Identify the blood parasite species.
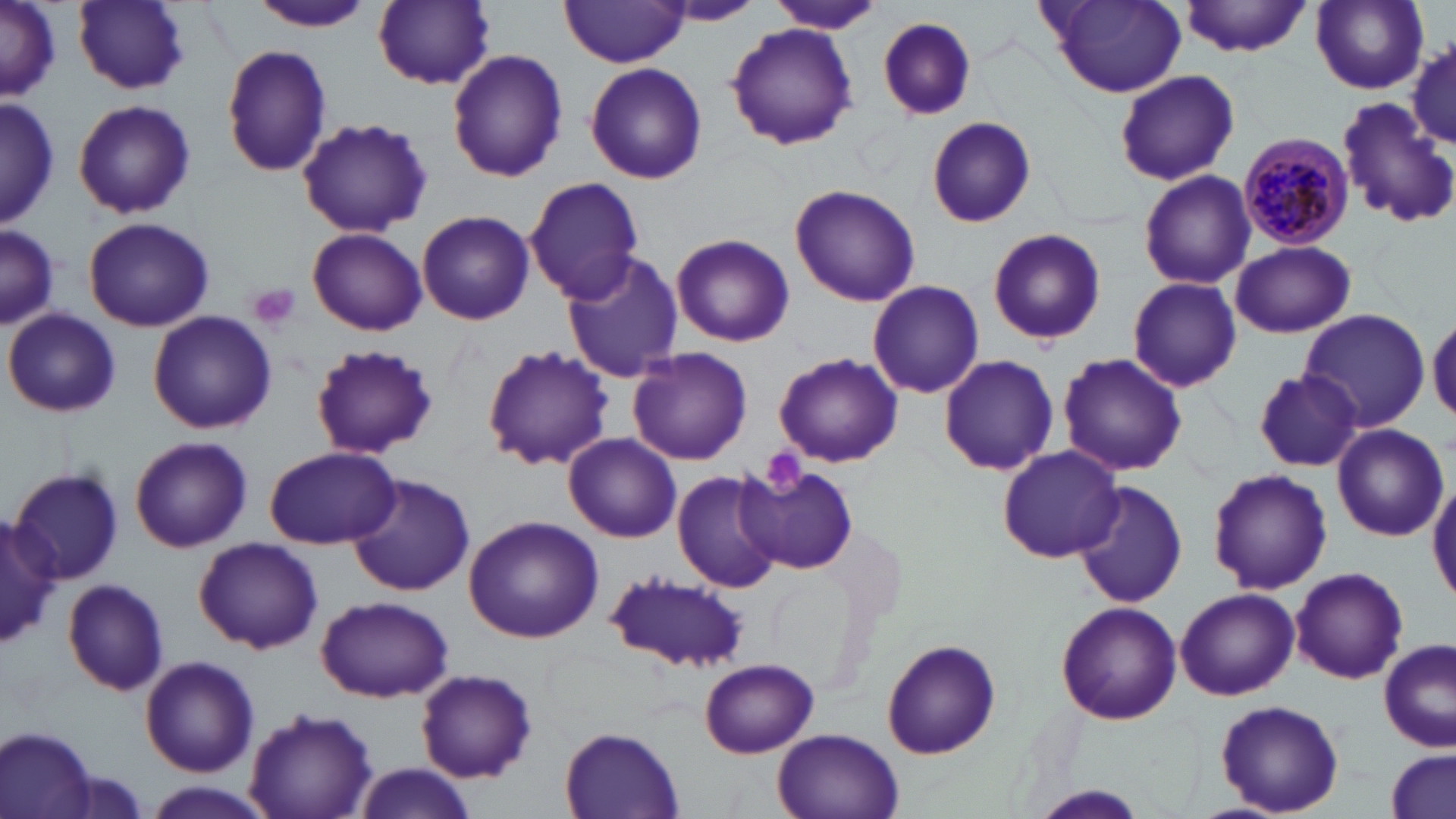
Plasmodium malariae.

Approximate bounding boxes as (x1,y1)-(x2,y2) corner pairs in pixels. Uninfected red blood cell locations: (0,0)-(59,103), (246,0)-(375,31), (373,0)-(496,88), (1042,0)-(1188,97), (1311,0)-(1429,92), (73,1)-(191,93), (1184,1)-(1312,56), (561,2)-(690,67), (666,2)-(763,24), (768,2)-(886,35), (879,16)-(978,120), (726,23)-(857,151), (1407,38)-(1456,151), (221,43)-(333,178), (446,49)-(569,182), (586,61)-(707,186), (1113,70)-(1240,184), (0,97)-(58,230), (1334,97)-(1455,230), (73,98)-(196,220), (928,116)-(1036,228), (296,118)-(433,238), (1138,169)-(1256,290), (525,176)-(647,303), (789,185)-(919,307), (417,209)-(535,325), (83,217)-(216,332), (0,226)-(59,329), (987,227)-(1106,346), (307,228)-(427,337), (671,233)-(794,347), (1229,240)-(1355,339), (560,250)-(684,382), (1127,276)-(1243,392), (869,281)-(984,399), (5,308)-(120,418), (1298,309)-(1430,431), (147,311)-(277,434), (1428,313)-(1456,422), (308,343)-(438,459), (481,344)-(614,471), (626,348)-(753,465), (1057,352)-(1187,477), (774,354)-(903,467), (937,355)-(1060,475), (1252,369)-(1364,471), (1333,423)-(1447,541), (563,434)-(683,544), (129,437)-(252,552), (265,445)-(401,549), (997,445)-(1124,563), (11,466)-(123,585), (1208,466)-(1332,594), (672,468)-(785,593), (744,469)-(860,572), (345,473)-(476,596), (1429,478)-(1456,601), (1073,481)-(1187,608), (464,515)-(604,643), (1,516)-(60,654), (194,537)-(324,655), (1290,568)-(1409,684), (605,572)-(751,671), (63,579)-(171,694), (1176,586)-(1299,700), (318,595)-(452,702), (1057,602)-(1181,723), (883,640)-(1000,759), (1378,640)-(1453,751), (140,655)-(259,776), (701,659)-(818,758), (416,668)-(536,782), (1214,700)-(1344,817), (244,705)-(378,818), (1,726)-(102,819), (560,728)-(682,819), (776,731)-(900,819), (1385,750)-(1454,819), (350,764)-(480,819), (146,782)-(267,816), (1024,788)-(1155,819). Plasmodium malariae-infected red blood cell locations: (1237,132)-(1355,250). Platelet locations: (246,283)-(302,332), (760,448)-(809,496). Thin blood smear. May-Grünwald-Giemsa-stained preparation. Single field of view. 1000x magnification. Image is 1456×819 pixels. Light microscopy.